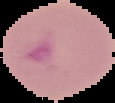

Image is 115×103 pixels. Result: malaria parasites identified. Cell region segmented out of the field of view; the surrounding area is masked to black. From a thin blood film.